Assess the morphology of the red blood cells.
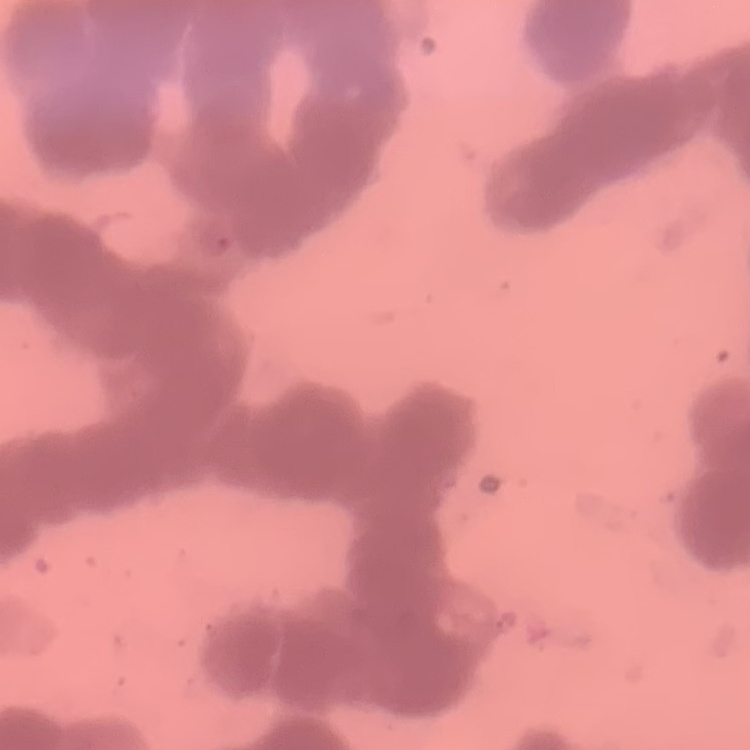

Rouleaux formation.

stain = Field's or Giemsa
image type = one tile cut from a larger photomicrograph
preparation = thin peripheral smear